Report the malaria status of this cell.
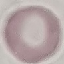
Uninfected.

Summary:
  - Preparation: thin blood film
  - Capture: smartphone through the microscope eyepiece
  - Image type: cell patch, automatically extracted from a larger field of view and resized to 64 × 64 pixels
  - Stain: Giemsa